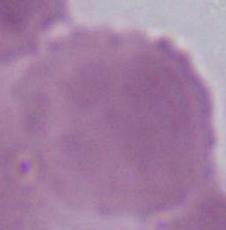
magnification = 1000x
modality = micrograph
identification = red blood cell